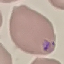
Summary:
  - Result: malaria parasites identified
  - Image type: automatically extracted cell patch, resized to 64 × 64 pixels
  - Preparation: thin smear
  - Capture: smartphone through the microscope eyepiece
  - Stain: Giemsa